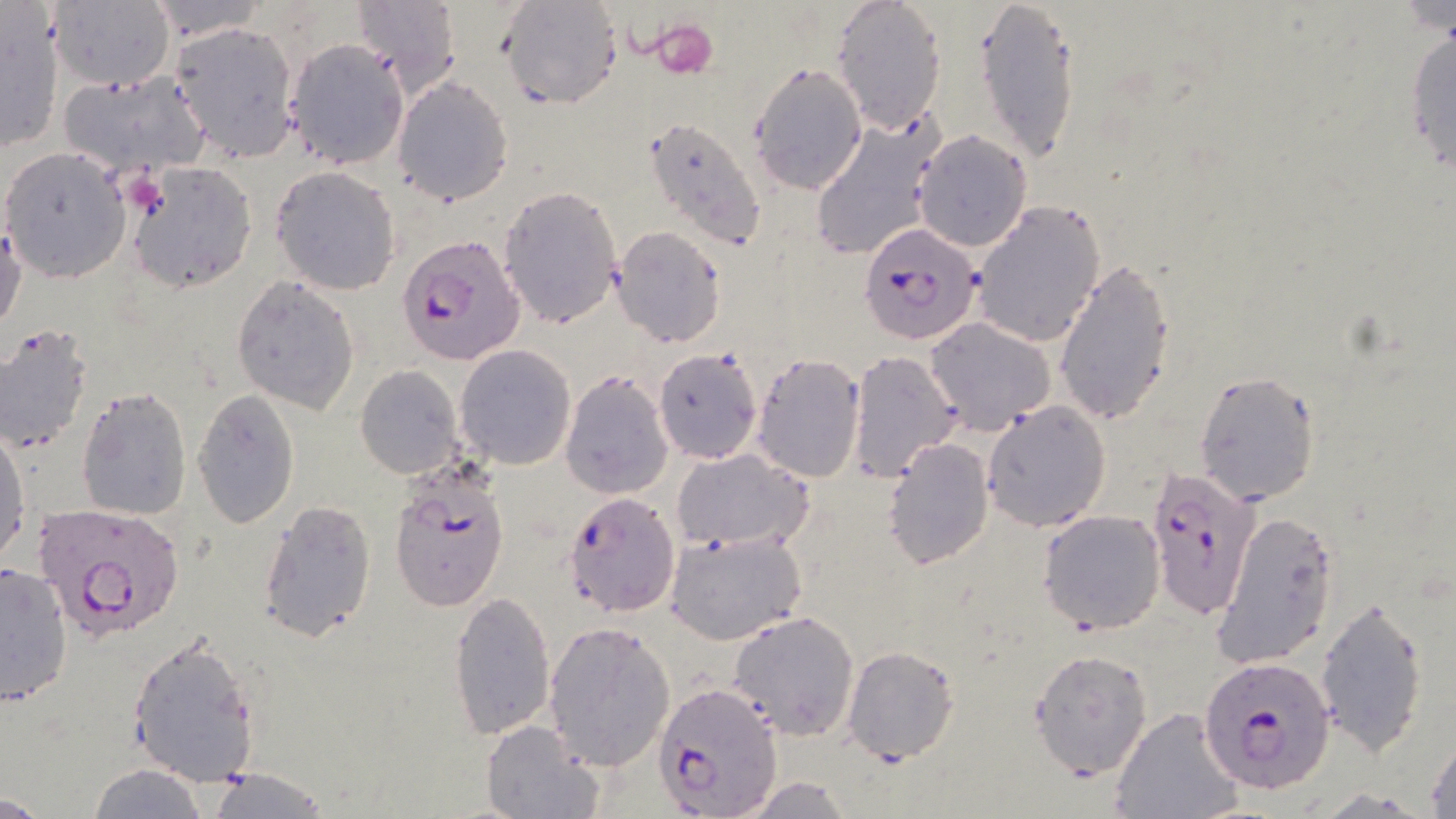
slide-level diagnosis = Plasmodium falciparum
uninfected red blood cell locations = approximate bounding boxes as (x1, y1, x2, y2) in pixels: (144, 0, 268, 40), (349, 0, 463, 95), (497, 0, 624, 111), (973, 0, 1080, 164), (48, 1, 175, 91), (830, 1, 946, 134), (1392, 2, 1456, 39), (0, 8, 64, 156), (1404, 19, 1456, 184), (171, 22, 301, 162), (284, 40, 409, 169), (747, 62, 868, 195), (56, 72, 212, 176), (392, 76, 513, 205), (807, 116, 942, 263), (645, 118, 768, 251), (912, 129, 1033, 251), (1, 147, 132, 284), (128, 161, 258, 294), (270, 165, 401, 296), (497, 185, 623, 330), (970, 199, 1106, 348), (1, 219, 26, 334), (613, 228, 726, 348), (1054, 256, 1177, 425), (232, 276, 360, 415), (924, 318, 1056, 433), (0, 324, 94, 455), (454, 344, 577, 468), (654, 347, 761, 464), (848, 352, 961, 481), (751, 353, 868, 483), (355, 365, 464, 478), (1194, 370, 1321, 506), (560, 372, 673, 499), (77, 387, 191, 520), (192, 391, 301, 528), (982, 400, 1111, 532), (1, 427, 30, 564), (882, 436, 994, 568), (673, 449, 813, 555), (257, 497, 378, 643), (1037, 508, 1165, 632), (1211, 511, 1339, 670), (664, 529, 808, 645), (0, 560, 75, 710), (448, 590, 556, 741), (1315, 598, 1430, 754), (454, 602, 659, 752), (728, 609, 860, 740), (543, 620, 675, 772), (127, 635, 260, 786), (843, 646, 960, 764), (1028, 648, 1154, 780), (1109, 706, 1243, 818), (480, 719, 601, 819), (1427, 736, 1456, 818), (89, 763, 207, 818), (199, 765, 331, 819), (734, 776, 857, 816), (0, 793, 52, 819)
stain = May-Grünwald-Giemsa
field of view = one of a larger specimen
image size = 1456×819 pixels
Plasmodium falciparum-infected red blood cell locations = approximate bounding boxes as (x1, y1, x2, y2) in pixels: (859, 222, 984, 344), (398, 235, 521, 365), (1147, 465, 1261, 621), (388, 466, 511, 614), (563, 489, 681, 619), (33, 501, 185, 642), (1198, 656, 1335, 794), (655, 683, 779, 816)
platelet locations = approximate bounding boxes as (x1, y1, x2, y2) in pixels: (648, 18, 720, 77), (124, 170, 171, 219)
modality = optical microscopy
magnification = 1000x
preparation = thin blood smear